Locate every blood parasite and identify its species.
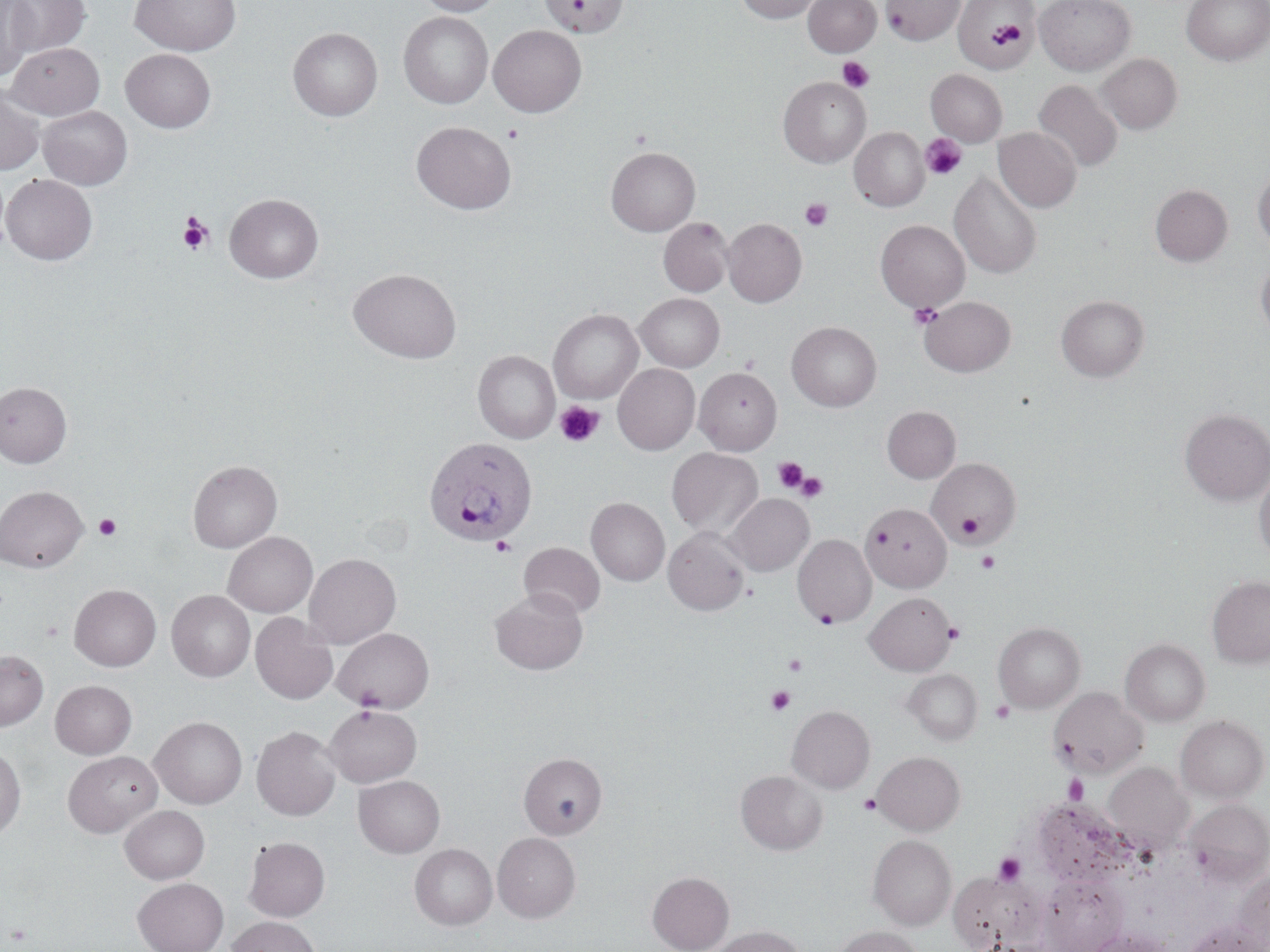
Approximate bounding boxes as (x1, y1, x2, y2) in pixels.
Plasmodium ovale-infected red blood cells: (424, 437, 538, 546).
No Plasmodium falciparum, Plasmodium malariae, Plasmodium vivax, Babesia divergens, or Trypanosoma brucei observed.

Summary:
  - Uninfected red blood cell locations: (4, 0, 91, 57), (129, 0, 241, 56), (413, 0, 505, 16), (540, 0, 628, 37), (736, 0, 823, 23), (803, 0, 881, 57), (882, 0, 962, 45), (953, 0, 1039, 72), (1034, 0, 1137, 75), (1182, 0, 1269, 65), (0, 2, 35, 79), (399, 12, 493, 108), (488, 26, 586, 117), (288, 27, 383, 121), (6, 42, 105, 119), (121, 48, 216, 133), (1097, 53, 1182, 134), (926, 69, 1007, 146), (778, 76, 871, 168), (1033, 80, 1122, 172), (0, 83, 45, 175), (38, 106, 132, 189), (411, 121, 516, 214), (850, 127, 929, 211), (993, 127, 1081, 212), (606, 146, 700, 236), (1253, 168, 1270, 252), (949, 170, 1042, 279), (1, 174, 97, 265), (1150, 184, 1233, 266), (225, 194, 323, 283), (658, 217, 734, 297), (722, 218, 807, 307), (875, 219, 970, 313), (1256, 258, 1270, 342), (349, 268, 461, 363), (636, 293, 724, 371), (1056, 294, 1149, 381), (920, 296, 1016, 376), (549, 309, 643, 403), (787, 322, 882, 411), (473, 350, 560, 443), (613, 364, 700, 454), (694, 367, 781, 454), (0, 381, 72, 467), (882, 406, 960, 483), (1179, 408, 1270, 506), (667, 447, 763, 539), (928, 458, 1020, 544), (188, 460, 282, 552), (1254, 467, 1270, 562), (0, 485, 88, 571), (725, 493, 813, 575), (586, 497, 669, 586), (862, 502, 951, 592), (663, 527, 750, 615), (223, 532, 317, 617), (793, 534, 876, 627), (519, 542, 605, 619), (304, 553, 401, 648), (1207, 576, 1270, 668), (69, 584, 161, 671), (491, 589, 587, 675), (167, 590, 255, 682), (865, 592, 956, 675), (250, 612, 338, 705), (993, 622, 1085, 713), (332, 627, 434, 713), (1121, 639, 1209, 725), (0, 650, 48, 730), (904, 668, 982, 744), (51, 680, 137, 759), (1048, 687, 1148, 778), (324, 705, 422, 787), (787, 705, 874, 793), (1176, 715, 1268, 803), (150, 716, 247, 808), (252, 726, 341, 820), (0, 745, 26, 839), (63, 751, 162, 837), (873, 751, 964, 834), (519, 753, 607, 838), (1104, 762, 1193, 854), (735, 770, 827, 855), (354, 775, 445, 858), (1028, 798, 1139, 889), (1184, 799, 1270, 885), (120, 805, 209, 883), (493, 832, 580, 923), (868, 835, 956, 930), (244, 836, 330, 921), (410, 843, 497, 930), (1232, 870, 1270, 950), (647, 871, 734, 952), (949, 874, 1046, 952), (1042, 876, 1126, 952), (133, 878, 228, 952), (226, 916, 322, 952), (1184, 921, 1266, 952), (710, 925, 804, 952), (834, 926, 924, 952), (1085, 928, 1173, 952)
  - Platelet locations: (989, 20, 1029, 54), (837, 57, 875, 93), (503, 124, 523, 143), (920, 133, 966, 181), (799, 198, 833, 232), (177, 213, 214, 254), (908, 302, 942, 329), (555, 400, 605, 447), (773, 456, 808, 493), (796, 472, 828, 502), (956, 512, 983, 544), (94, 514, 121, 540), (491, 536, 516, 556), (976, 550, 1000, 574), (813, 607, 840, 628), (944, 621, 964, 643), (783, 653, 808, 676), (766, 686, 795, 714), (990, 700, 1015, 723), (1063, 774, 1088, 804), (858, 794, 880, 815), (992, 853, 1027, 886)
  - Slide-level diagnosis: Plasmodium ovale
  - Image size: 1270×952 pixels
  - Stain: May-Grünwald-Giemsa
  - Magnification: 1000x
  - Preparation: thin blood smear
  - Field of view: single
  - Modality: optical microscopy